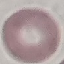
result = no malaria parasites detected
preparation = thin smear
stain = Giemsa
image type = cell patch, automatically extracted from a larger field of view and resized to 64 × 64 pixels
capture = smartphone through the microscope eyepiece